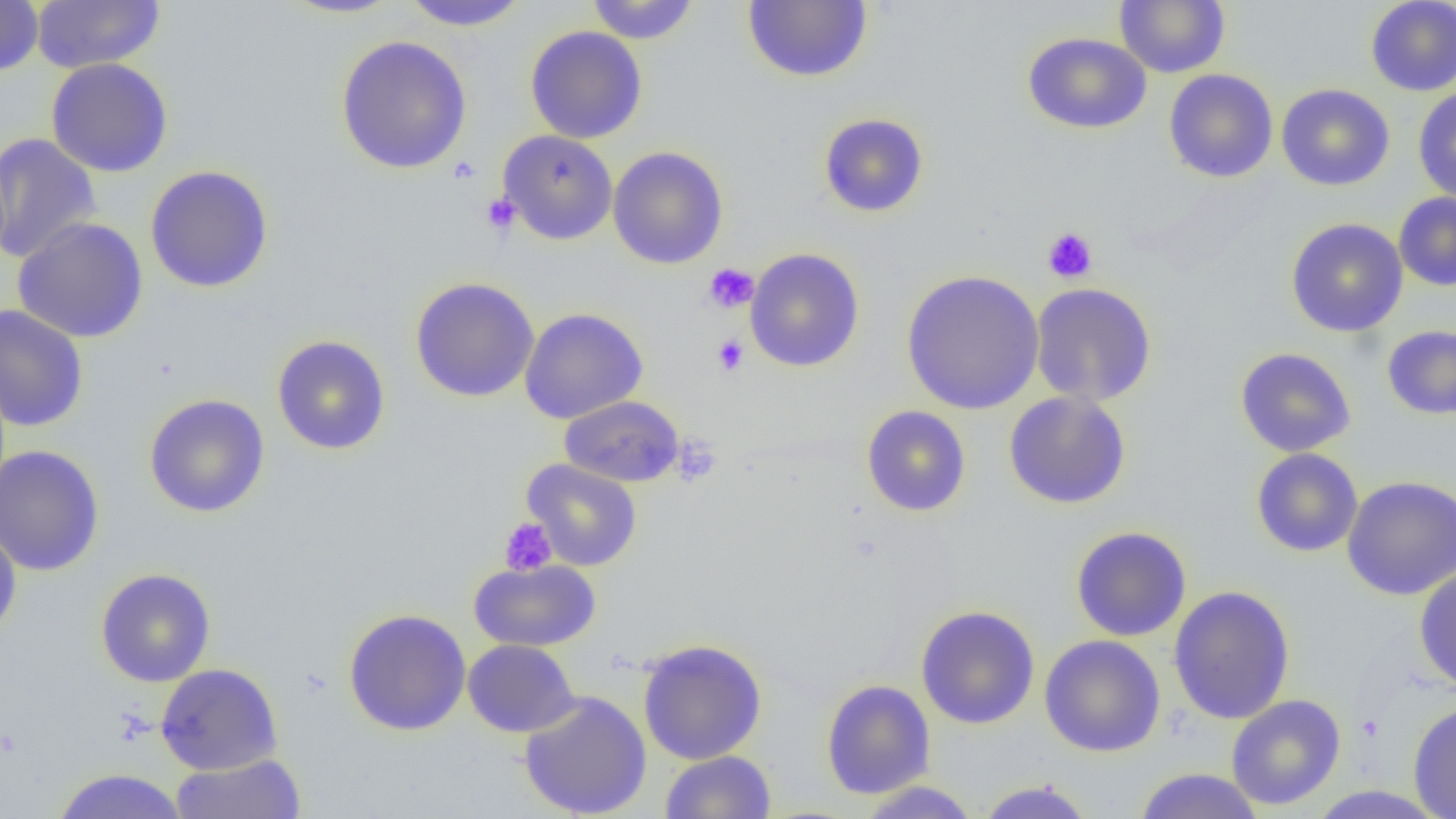

Summary:
  - Coordinate format: approximate bounding boxes as (x1, y1, x2, y2) in pixels
  - Uninfected red blood cell locations: (32, 0, 164, 73), (280, 0, 404, 19), (400, 0, 528, 31), (585, 0, 700, 44), (741, 0, 873, 84), (1115, 0, 1230, 78), (1365, 0, 1456, 96), (0, 1, 44, 77), (524, 26, 647, 143), (1022, 32, 1152, 134), (335, 34, 472, 174), (46, 58, 173, 177), (1164, 69, 1278, 183), (1276, 83, 1394, 192), (1413, 86, 1456, 204), (818, 112, 929, 218), (498, 130, 618, 245), (0, 132, 101, 264), (608, 146, 728, 269), (145, 164, 274, 293), (1394, 193, 1456, 291), (12, 217, 149, 343), (1285, 218, 1408, 337), (744, 248, 865, 372), (901, 269, 1044, 415), (410, 277, 540, 402), (1030, 282, 1157, 407), (0, 305, 89, 432), (519, 307, 648, 424), (1382, 324, 1456, 420), (271, 335, 390, 455), (1235, 347, 1356, 457), (1003, 391, 1132, 509), (144, 394, 270, 518), (560, 395, 684, 487), (861, 405, 971, 517), (0, 444, 104, 577), (1251, 448, 1363, 557), (521, 458, 642, 571), (1341, 475, 1456, 600), (0, 523, 22, 643), (1070, 526, 1192, 641), (469, 559, 601, 651), (1414, 566, 1456, 691), (96, 568, 215, 687), (1169, 585, 1295, 724), (915, 605, 1040, 729), (343, 608, 472, 736), (1039, 634, 1166, 757), (637, 638, 767, 765), (463, 639, 580, 737), (155, 663, 283, 775), (820, 679, 935, 799), (519, 690, 652, 818), (1226, 694, 1346, 810), (1408, 700, 1456, 819), (660, 750, 776, 819), (170, 753, 306, 819), (51, 768, 188, 819), (1133, 768, 1265, 819), (974, 779, 1097, 819), (855, 780, 982, 818)
  - Platelet locations: (480, 192, 521, 237), (1042, 226, 1098, 284), (703, 263, 759, 313), (712, 334, 749, 377), (671, 436, 721, 487), (499, 517, 557, 576)
  - Slide-level diagnosis: no evidence of blood parasites
  - Image size: 1456×819 pixels
  - Magnification: 1000x
  - Field of view: one of a larger specimen
  - Modality: light microscopy
  - Preparation: thin blood film